Name the parasite shown.
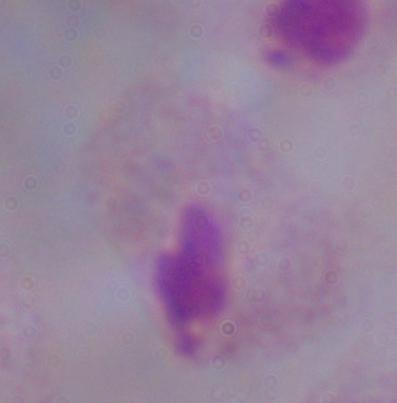

This is a trichomonad.

Summary:
  - Modality: photomicrograph
  - Magnification: 1000x